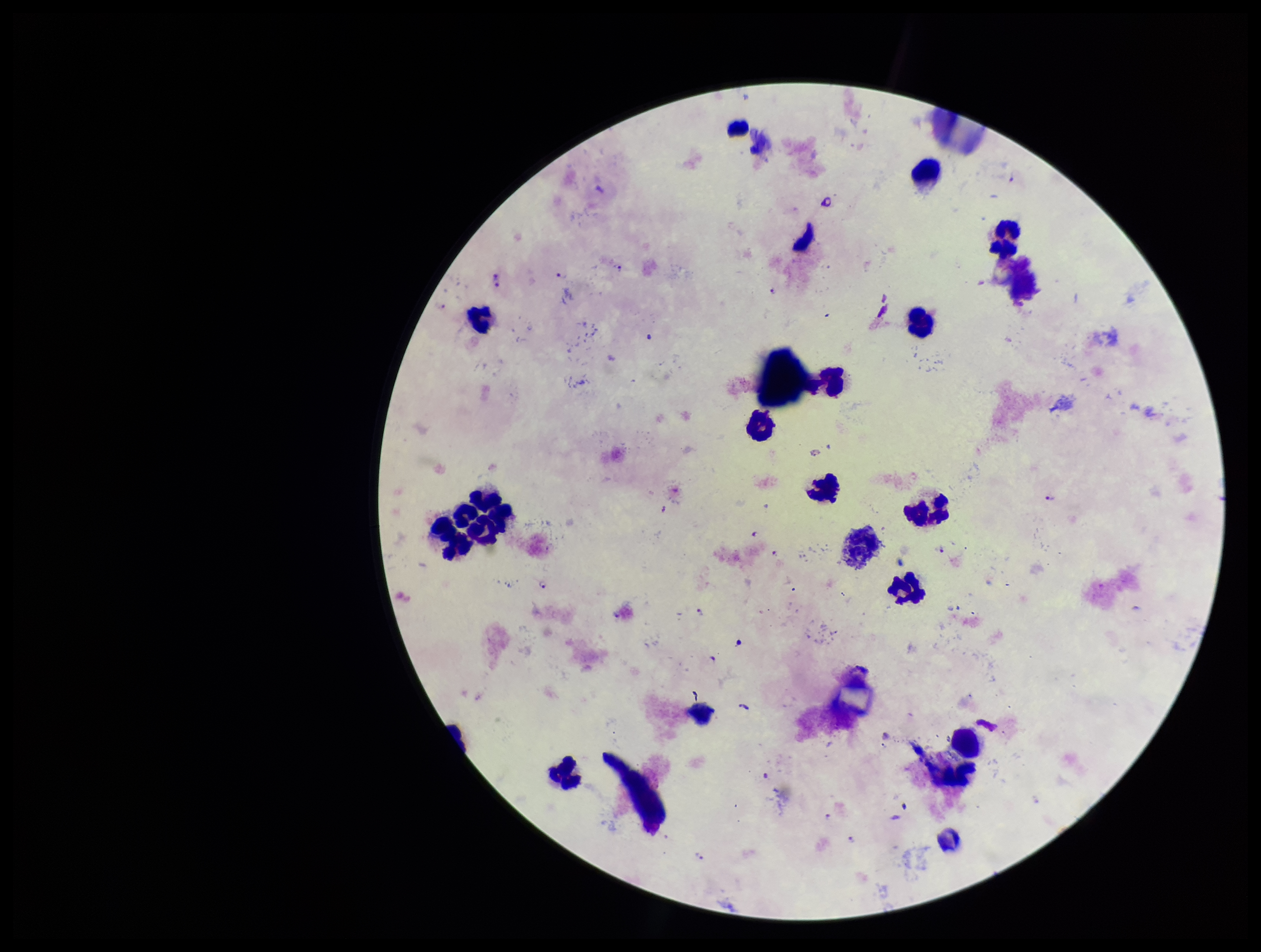

preparation = thick
image size = 1261×952 pixels
leukocyte count = 20
capture = smartphone photograph through the microscope eyepiece
stain = Giemsa
patient malaria status = infected
field of view = single
species reported for this patient = Plasmodium falciparum
parasite count = 11
Plasmodium parasites = seen